Assess this cell for malaria.
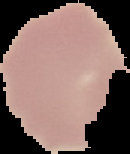
Uninfected.

Image is 130×154 pixels. From a thin blood film. The area outside the segmented cell region is set to black.